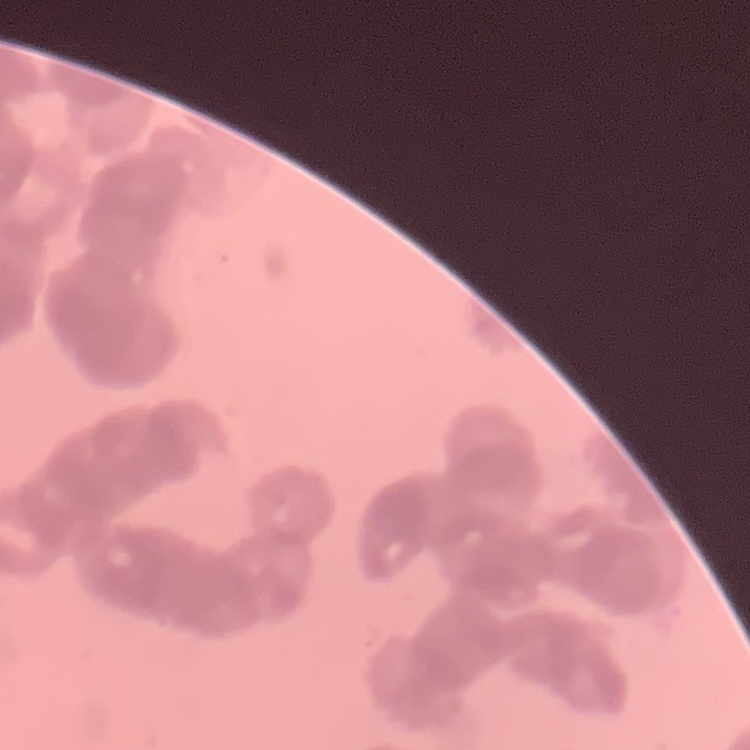

The erythrocytes show rouleaux formation. Thin blood smear. Field's or Giemsa stain. Square crop of a larger photomicrograph.